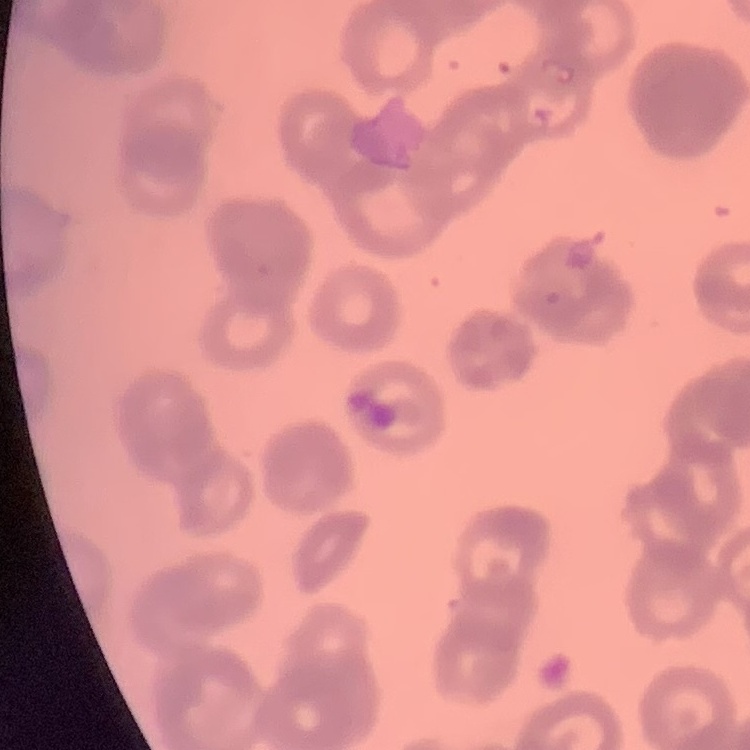

The erythrocytes show rouleaux formation. Field's or Giemsa stain. Thin blood film. Square crop of a larger photomicrograph.